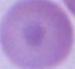
1000x magnification. A red blood cell is shown. Photomicrograph.